Name the cell type shown.
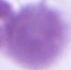
An erythrocyte.

{
  "modality": "micrograph",
  "magnification": "1000x"
}